Classify this cell by malaria status.
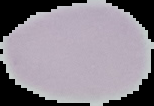

Uninfected.

Segmented cell region on a black background. Image is 154×106 pixels. From a thin blood film.